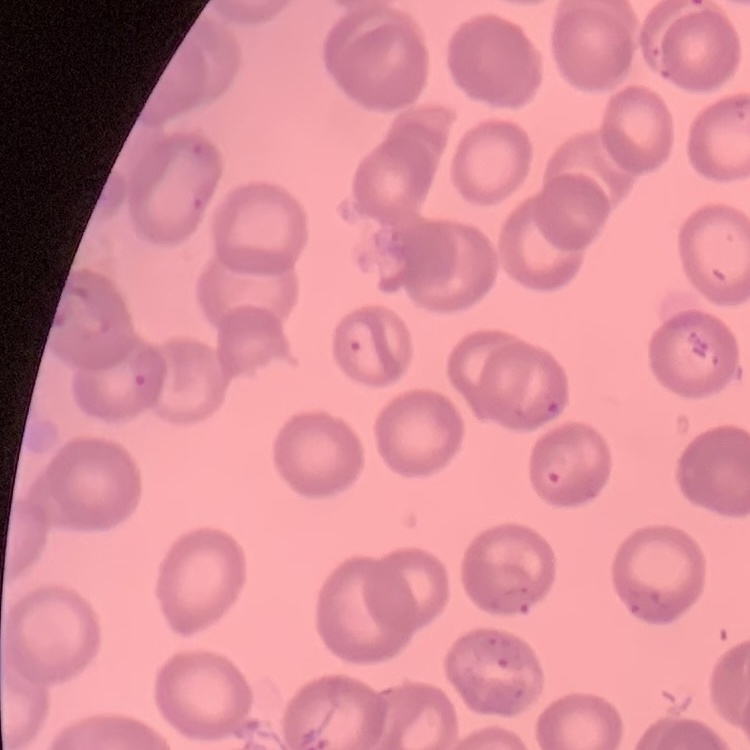 The red blood cells show no rouleaux formation. Thin blood film. One tile cut from a larger photomicrograph. Stained with either Field's or Giemsa.